Locate and identify every blood parasite.
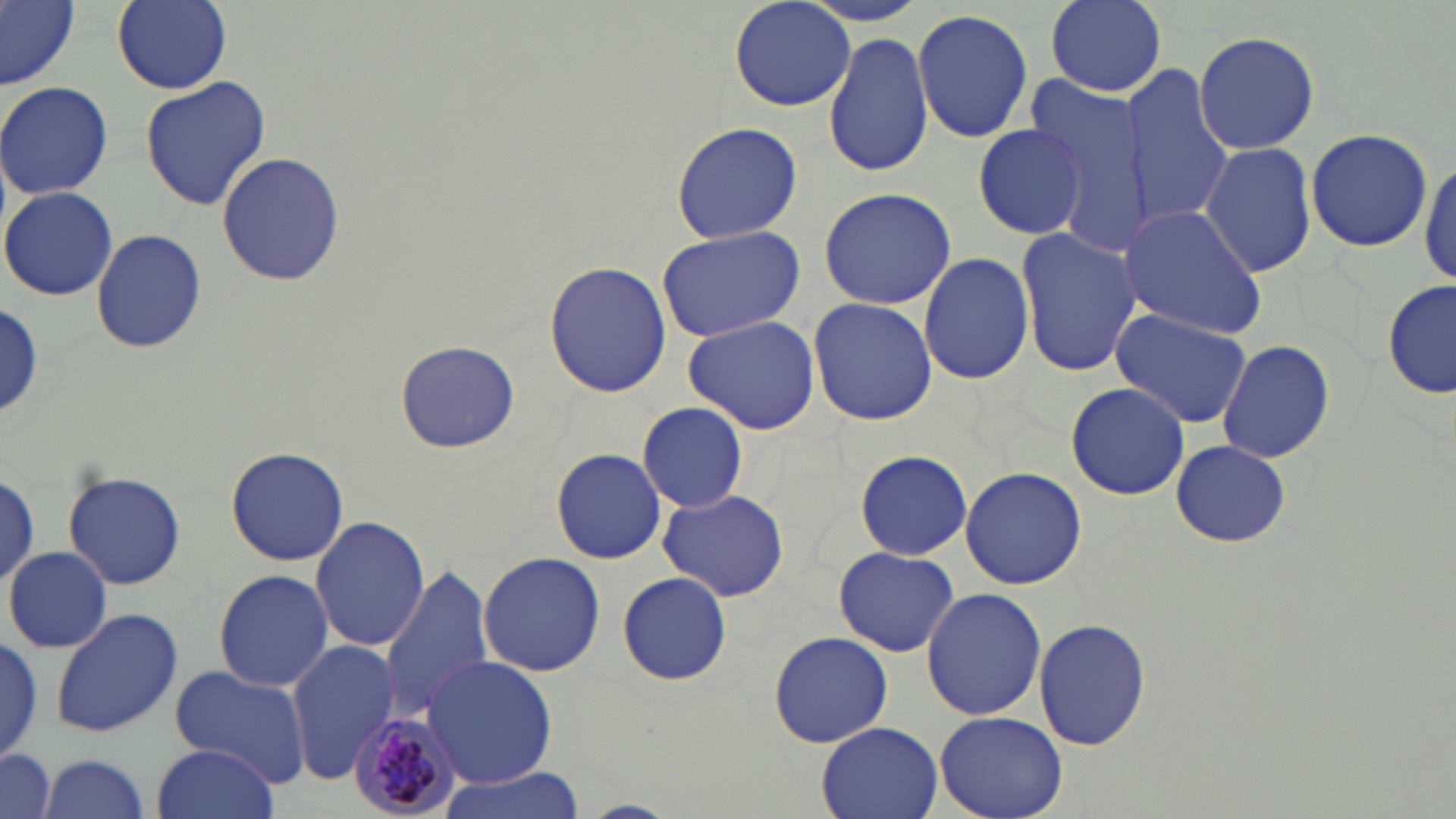

Approximate bounding boxes as (x1, y1, x2, y2) in pixels.
Plasmodium malariae-infected red blood cells: (347, 709, 463, 819).
No Plasmodium falciparum, Plasmodium ovale, Plasmodium vivax, Babesia divergens, or Trypanosoma brucei observed.

Summary:
  - Uninfected red blood cell locations: (0, 0, 78, 90), (113, 0, 231, 93), (729, 0, 857, 111), (1043, 0, 1167, 95), (912, 8, 1033, 143), (1193, 29, 1320, 155), (825, 30, 935, 179), (1124, 68, 1235, 228), (139, 76, 270, 211), (0, 81, 113, 200), (1026, 81, 1148, 247), (972, 120, 1091, 243), (671, 122, 802, 244), (1305, 129, 1432, 251), (1198, 140, 1317, 280), (217, 151, 345, 286), (1419, 156, 1455, 291), (2, 186, 117, 301), (817, 187, 955, 311), (1121, 205, 1269, 338), (655, 225, 806, 343), (1017, 227, 1141, 379), (91, 229, 208, 354), (918, 250, 1032, 387), (545, 259, 671, 398), (1382, 279, 1456, 403), (808, 297, 938, 427), (1, 300, 47, 420), (1109, 307, 1254, 429), (683, 315, 819, 433), (395, 339, 519, 454), (1215, 339, 1336, 464), (1065, 383, 1192, 500), (637, 401, 748, 514), (1169, 441, 1291, 546), (552, 445, 667, 564), (226, 446, 349, 567), (855, 450, 971, 561), (960, 467, 1089, 589), (0, 472, 40, 589), (63, 472, 187, 588), (658, 487, 789, 603), (310, 515, 430, 653), (833, 545, 960, 658), (5, 546, 111, 654), (478, 552, 607, 677), (378, 564, 493, 723), (213, 568, 334, 692), (618, 573, 732, 685), (921, 587, 1047, 722), (50, 606, 183, 739), (1034, 617, 1152, 753), (0, 629, 43, 762), (769, 631, 892, 748), (0, 634, 44, 763), (285, 642, 401, 781), (424, 655, 557, 789), (171, 664, 312, 786), (935, 709, 1069, 818), (815, 722, 943, 819), (152, 744, 280, 819), (0, 747, 58, 819), (35, 753, 153, 819), (434, 767, 586, 819)
  - Slide-level diagnosis: Plasmodium malariae
  - Image size: 1456×819 pixels
  - Stain: May-Grünwald-Giemsa
  - Field of view: one of a larger specimen
  - Preparation: thin blood film
  - Modality: light microscopy
  - Magnification: 1000x